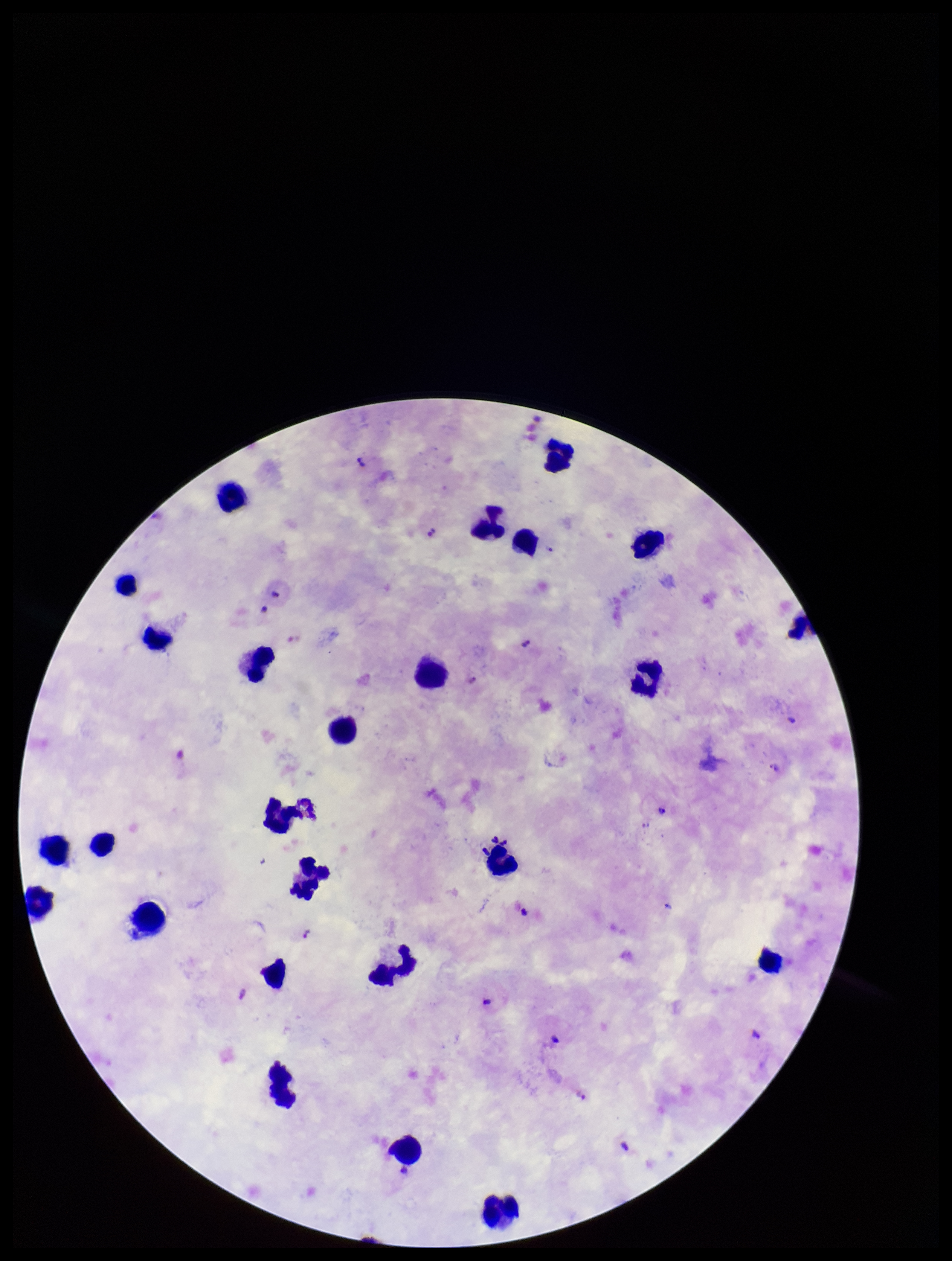
{
  "parasite_count": 13,
  "patient_malaria_status": "positive",
  "preparation": "thick blood smear",
  "plasmodium_parasites": "detected",
  "leukocyte_count": 25,
  "image_size": "952×1261 pixels",
  "stain": "Giemsa",
  "species_reported_for_this_patient": "Plasmodium falciparum",
  "capture": "smartphone photograph through the microscope eyepiece",
  "field_of_view": "single"
}